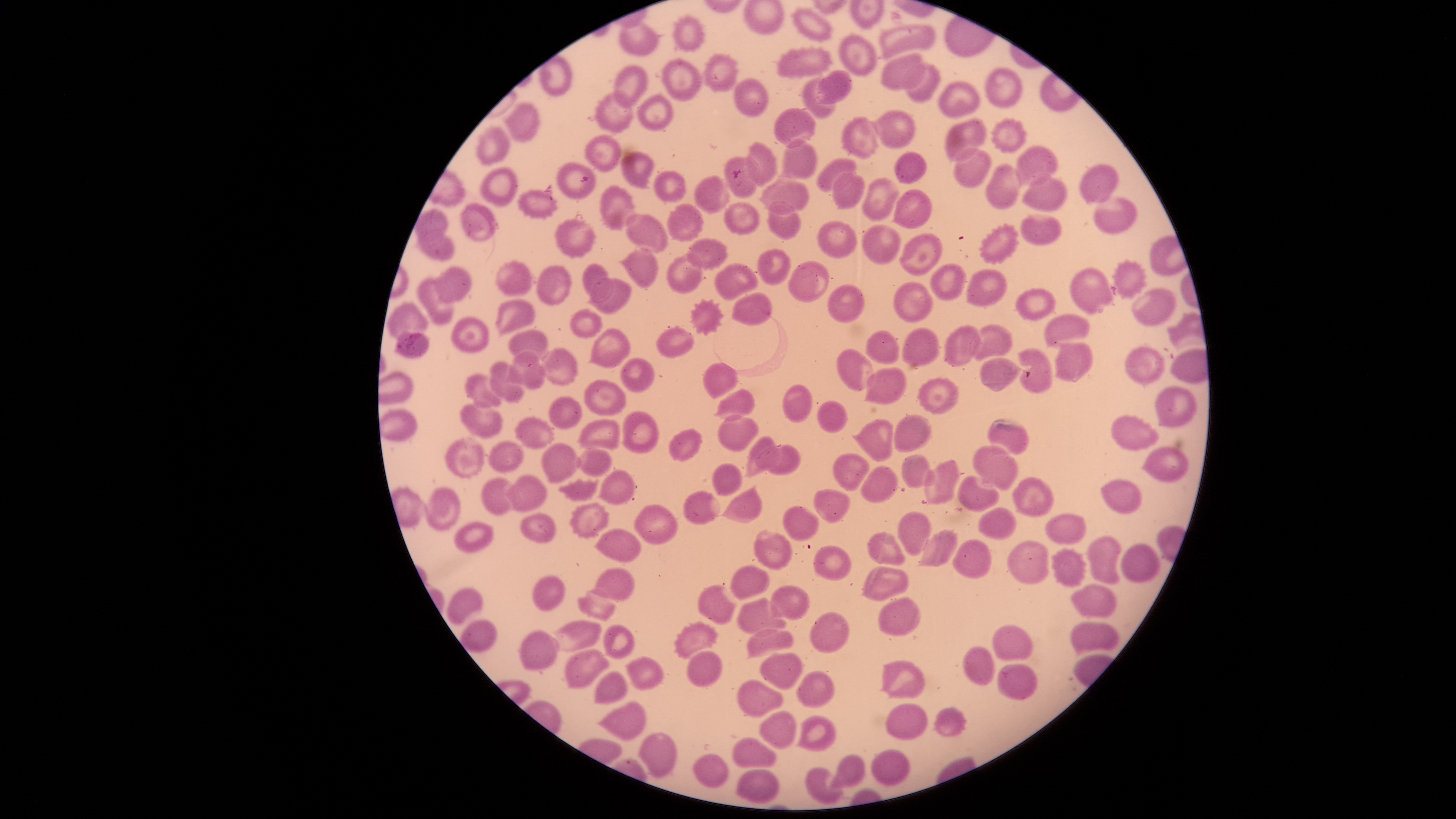
parasitized red blood cells = approximate bounding boxes as [left, top, right, bottom] in pixels: [395, 330, 430, 358], [980, 358, 1022, 393]
visible region = circular
capture = smartphone photograph through the microscope eyepiece
presence = malaria parasites identified
preparation = thin blood film
field of view = single
uninfected red blood cells = approximate bounding boxes as [left, top, right, bottom] in pixels: [792, 8, 832, 41], [673, 15, 703, 52], [620, 22, 660, 56], [880, 25, 936, 57], [840, 34, 877, 75], [778, 47, 832, 77], [881, 52, 926, 90], [704, 54, 737, 92], [662, 58, 701, 101], [903, 64, 940, 102], [613, 65, 648, 109], [986, 68, 1023, 107], [816, 69, 851, 103], [735, 79, 767, 116], [802, 79, 835, 118], [938, 81, 979, 116], [596, 93, 632, 132], [638, 95, 673, 132], [505, 102, 538, 142], [775, 110, 815, 147], [869, 111, 914, 147], [842, 116, 878, 159], [992, 118, 1025, 154], [945, 119, 987, 164], [477, 127, 509, 164], [587, 136, 620, 171], [780, 140, 816, 179], [747, 143, 776, 186], [1015, 145, 1058, 187], [953, 149, 991, 188], [894, 151, 928, 183], [622, 152, 654, 188], [725, 158, 756, 199], [818, 159, 856, 191], [558, 163, 596, 200], [987, 165, 1019, 208], [1079, 165, 1118, 203], [480, 169, 517, 206], [654, 171, 686, 202], [831, 173, 864, 209], [696, 176, 730, 213], [862, 177, 900, 221], [1022, 177, 1066, 210], [760, 180, 808, 213], [601, 187, 635, 229], [519, 189, 557, 218], [892, 190, 932, 229], [1092, 196, 1138, 234], [767, 201, 798, 240], [725, 203, 759, 237], [460, 204, 499, 240], [668, 204, 703, 241], [417, 210, 447, 240], [1021, 214, 1062, 244], [626, 215, 669, 253], [555, 219, 594, 260], [818, 221, 857, 258], [979, 224, 1018, 265], [862, 226, 900, 264], [900, 233, 942, 275], [419, 234, 454, 260], [688, 239, 729, 271], [756, 249, 791, 286], [620, 250, 657, 288], [667, 254, 702, 292], [1114, 260, 1147, 300], [496, 261, 532, 295], [789, 262, 829, 302], [715, 263, 758, 301], [583, 264, 609, 299], [931, 264, 965, 299], [537, 266, 572, 306], [435, 267, 471, 303], [1071, 267, 1113, 314], [964, 270, 1006, 306], [587, 278, 631, 313], [418, 279, 454, 323], [895, 283, 933, 321], [827, 285, 865, 323], [1131, 289, 1175, 324], [1016, 290, 1056, 320], [731, 294, 774, 324], [690, 298, 724, 335], [495, 300, 535, 335], [387, 303, 430, 337], [569, 309, 602, 338], [1044, 315, 1090, 349], [453, 318, 487, 354], [974, 324, 1012, 360], [944, 326, 982, 365], [902, 327, 937, 365], [587, 328, 630, 368], [656, 328, 694, 356], [508, 330, 549, 358], [865, 331, 899, 363], [1055, 343, 1094, 380], [1124, 346, 1166, 386], [539, 347, 577, 387], [836, 347, 876, 392], [1019, 347, 1054, 394], [504, 351, 545, 389], [619, 359, 655, 392], [489, 362, 525, 402], [704, 363, 738, 398], [865, 367, 907, 405], [463, 373, 501, 409], [917, 377, 958, 415], [584, 380, 627, 416], [783, 383, 812, 422], [1154, 385, 1197, 426], [714, 389, 755, 420], [550, 399, 581, 429], [818, 400, 847, 433], [461, 405, 501, 439], [622, 412, 659, 453], [894, 414, 932, 451], [718, 415, 758, 452], [1112, 415, 1159, 450], [515, 418, 552, 449], [577, 420, 620, 450], [851, 420, 892, 460], [988, 420, 1028, 455], [670, 430, 703, 461], [745, 436, 780, 477], [446, 439, 484, 479], [488, 442, 522, 473], [541, 442, 582, 483], [755, 444, 800, 476], [972, 445, 1017, 490], [1141, 447, 1190, 482], [577, 449, 611, 477], [834, 453, 869, 490], [900, 453, 936, 490], [924, 460, 960, 505], [711, 463, 742, 496], [859, 466, 900, 503], [598, 469, 635, 504], [503, 475, 549, 512], [958, 476, 999, 514], [1013, 477, 1054, 518], [482, 478, 511, 515], [558, 478, 598, 501], [1101, 479, 1141, 513], [720, 484, 762, 524], [426, 488, 461, 531], [815, 489, 850, 523], [683, 491, 721, 525], [568, 503, 608, 539], [634, 506, 678, 544], [784, 506, 819, 542], [977, 508, 1017, 539], [898, 512, 931, 557], [521, 514, 555, 542], [1044, 515, 1086, 544], [456, 523, 493, 553], [917, 529, 958, 567], [754, 530, 792, 570], [595, 531, 642, 562], [866, 532, 904, 567], [1088, 535, 1121, 584], [953, 540, 991, 579], [1008, 543, 1048, 584], [1122, 543, 1160, 583], [813, 545, 852, 580], [1052, 547, 1086, 587], [730, 566, 769, 600], [861, 567, 910, 602], [595, 569, 633, 601], [532, 576, 564, 610], [1070, 584, 1117, 618], [769, 585, 810, 620], [698, 586, 736, 625], [447, 587, 483, 625], [577, 595, 616, 621], [878, 596, 922, 636], [738, 597, 786, 634], [808, 613, 849, 653], [459, 621, 497, 653], [553, 621, 602, 652], [675, 621, 718, 658], [1072, 622, 1119, 656], [604, 624, 634, 659], [993, 625, 1033, 660], [747, 629, 795, 658], [520, 631, 557, 669], [963, 646, 994, 686], [566, 650, 608, 688], [687, 651, 722, 686], [760, 654, 803, 689], [625, 658, 665, 690], [881, 661, 924, 699], [997, 664, 1037, 700], [796, 671, 836, 710], [593, 672, 627, 704], [738, 680, 784, 720], [596, 702, 645, 741], [886, 705, 929, 739], [931, 707, 967, 737], [760, 711, 796, 749], [796, 716, 836, 752], [636, 733, 677, 777], [732, 737, 776, 767], [871, 751, 909, 786], [692, 755, 729, 788], [827, 755, 866, 790], [805, 767, 842, 805], [735, 770, 779, 805]
image size = 1456×819 pixels
species = Plasmodium falciparum
stain = Giemsa